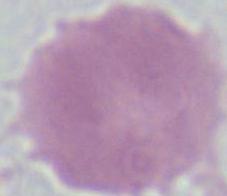
Summary:
  - Modality: photomicrograph
  - Identification: erythrocyte
  - Magnification: 1000x